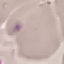
Malaria status: uninfected. Thin blood film. Cell patch, automatically extracted from a larger field of view and resized to 64 × 64 pixels. Giemsa-stained preparation. Acquired by smartphone through the microscope eyepiece.